Assess the morphology of the red blood cells.
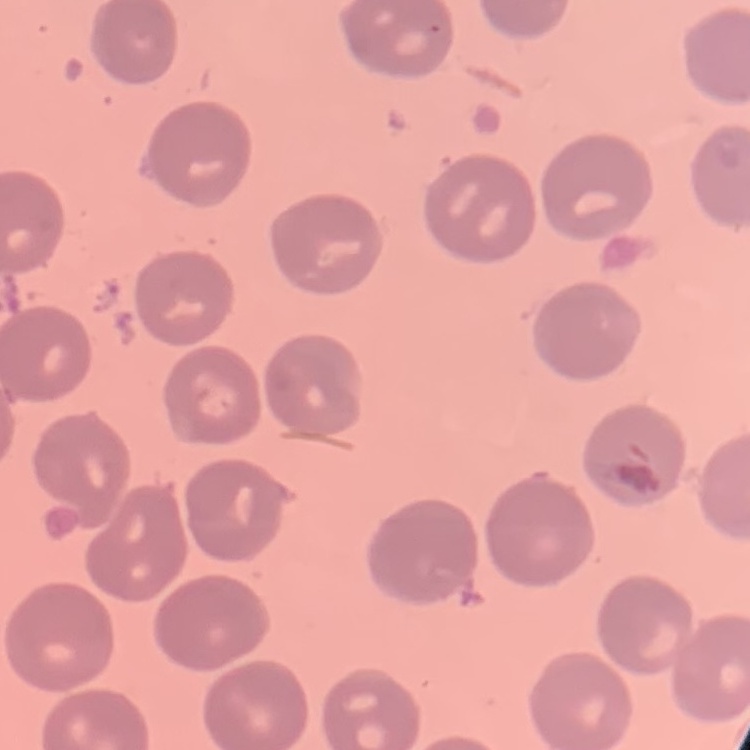

No rouleaux formation.

{
  "preparation": "thin blood smear",
  "image_type": "square crop of a larger photomicrograph",
  "stain": "Field's or Giemsa"
}